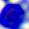 A white blood cell is seen. Captured at 400x magnification. Photomicrograph.